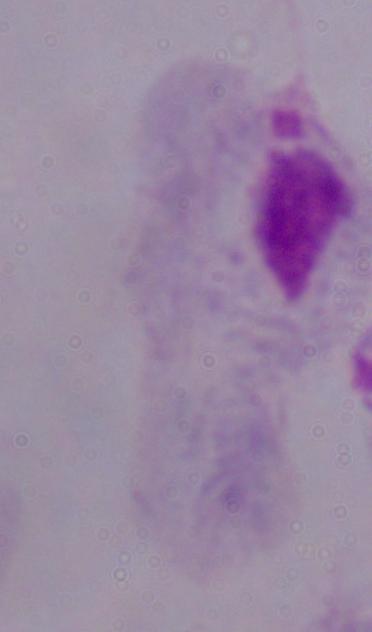

Summary:
  - Identification: trichomonad
  - Magnification: 1000x
  - Modality: photomicrograph